Report the malaria status of this cell.
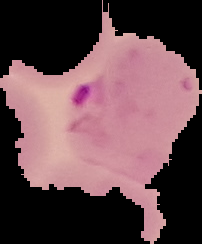
It is parasitized.

Image is 202×244 pixels. The area outside the segmented cell region is set to black. From a thin blood smear.